Outline each uninfected red blood cell.
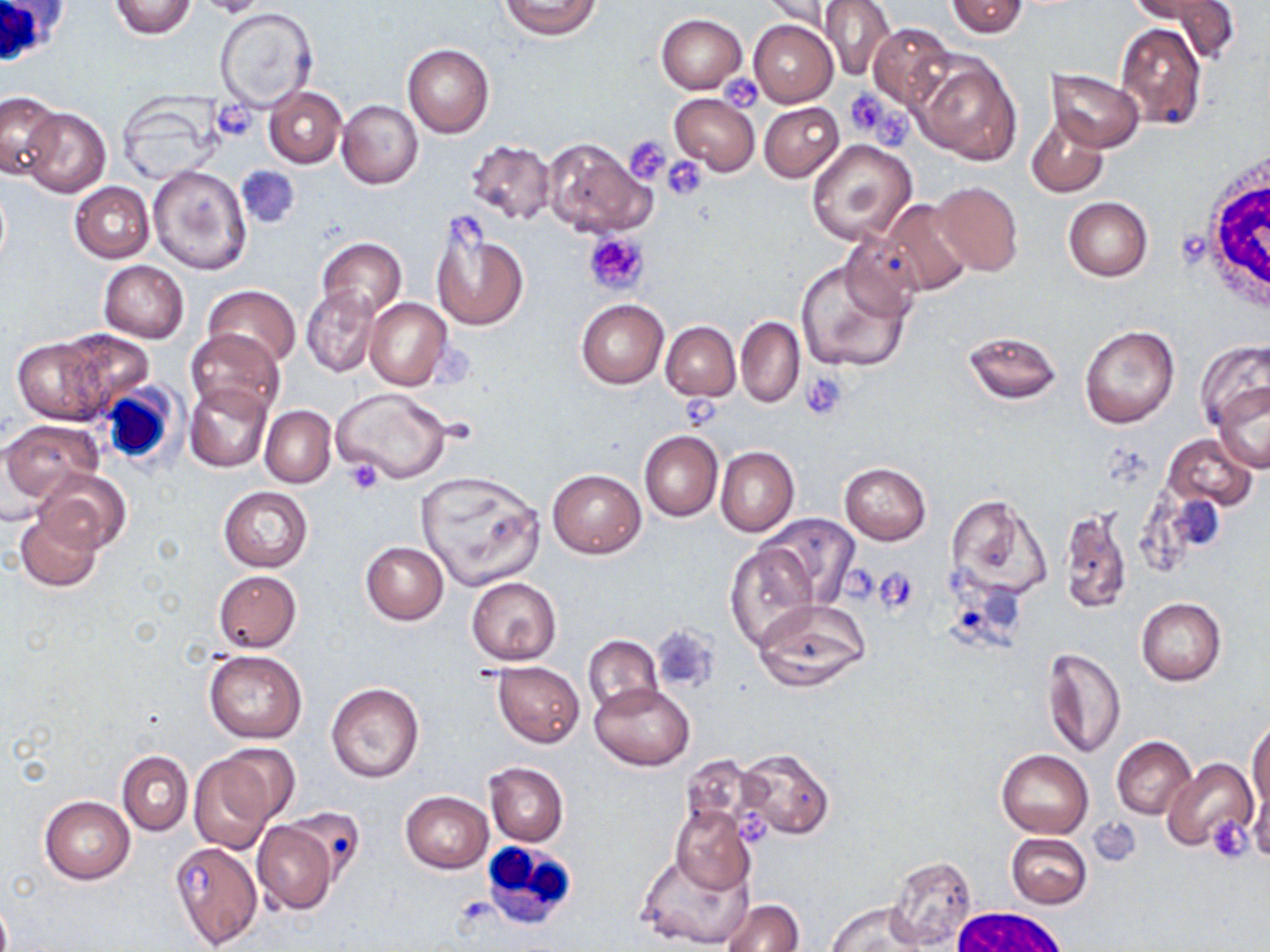

Approximate bounding boxes as named x1/y1/x2/y2 corners in pixels.
Uninfected red blood cells: (x1=108, y1=0, x2=197, y2=40), (x1=500, y1=0, x2=603, y2=42), (x1=760, y1=0, x2=845, y2=32), (x1=820, y1=0, x2=897, y2=83), (x1=945, y1=0, x2=1028, y2=37), (x1=1131, y1=0, x2=1226, y2=27), (x1=1147, y1=0, x2=1240, y2=61), (x1=215, y1=8, x2=317, y2=111), (x1=657, y1=14, x2=747, y2=93), (x1=749, y1=19, x2=838, y2=106), (x1=1116, y1=22, x2=1207, y2=130), (x1=868, y1=23, x2=953, y2=108), (x1=402, y1=44, x2=494, y2=137), (x1=913, y1=53, x2=1022, y2=165), (x1=1048, y1=69, x2=1144, y2=151), (x1=264, y1=87, x2=345, y2=167), (x1=0, y1=91, x2=63, y2=177), (x1=670, y1=93, x2=760, y2=176), (x1=116, y1=94, x2=221, y2=184), (x1=337, y1=100, x2=423, y2=189), (x1=759, y1=101, x2=843, y2=182), (x1=20, y1=108, x2=110, y2=197), (x1=1027, y1=115, x2=1110, y2=199), (x1=540, y1=137, x2=655, y2=239), (x1=464, y1=139, x2=557, y2=225), (x1=806, y1=139, x2=917, y2=246), (x1=235, y1=164, x2=302, y2=229), (x1=148, y1=165, x2=250, y2=274), (x1=933, y1=180, x2=1024, y2=276), (x1=70, y1=182, x2=155, y2=262), (x1=1064, y1=197, x2=1152, y2=282), (x1=880, y1=199, x2=974, y2=296), (x1=432, y1=223, x2=528, y2=332), (x1=838, y1=234, x2=924, y2=318), (x1=316, y1=237, x2=406, y2=322), (x1=796, y1=256, x2=910, y2=373), (x1=99, y1=260, x2=189, y2=342), (x1=301, y1=284, x2=381, y2=378), (x1=202, y1=285, x2=300, y2=369), (x1=364, y1=299, x2=452, y2=390), (x1=576, y1=299, x2=668, y2=389), (x1=736, y1=317, x2=804, y2=407), (x1=661, y1=322, x2=740, y2=400), (x1=1080, y1=325, x2=1181, y2=429), (x1=185, y1=327, x2=284, y2=420), (x1=54, y1=329, x2=154, y2=415), (x1=964, y1=329, x2=1062, y2=405), (x1=12, y1=337, x2=110, y2=424), (x1=1197, y1=339, x2=1270, y2=437), (x1=184, y1=383, x2=271, y2=472), (x1=1212, y1=383, x2=1270, y2=474), (x1=333, y1=387, x2=451, y2=485), (x1=260, y1=405, x2=335, y2=487), (x1=4, y1=419, x2=102, y2=503), (x1=639, y1=431, x2=723, y2=521), (x1=1163, y1=434, x2=1257, y2=511), (x1=716, y1=446, x2=799, y2=536), (x1=838, y1=462, x2=932, y2=544), (x1=36, y1=469, x2=130, y2=553), (x1=548, y1=469, x2=646, y2=558), (x1=415, y1=471, x2=548, y2=591), (x1=219, y1=487, x2=313, y2=572), (x1=944, y1=493, x2=1050, y2=601), (x1=1056, y1=506, x2=1133, y2=615), (x1=15, y1=510, x2=101, y2=592), (x1=760, y1=513, x2=859, y2=609), (x1=361, y1=541, x2=448, y2=624), (x1=726, y1=541, x2=815, y2=650), (x1=213, y1=570, x2=302, y2=653), (x1=478, y1=576, x2=569, y2=747), (x1=466, y1=578, x2=561, y2=665), (x1=1135, y1=596, x2=1226, y2=686), (x1=752, y1=600, x2=870, y2=691), (x1=582, y1=634, x2=662, y2=717), (x1=1043, y1=647, x2=1126, y2=759), (x1=205, y1=650, x2=306, y2=742), (x1=493, y1=662, x2=584, y2=747), (x1=590, y1=682, x2=694, y2=769), (x1=326, y1=683, x2=424, y2=784), (x1=1248, y1=718, x2=1270, y2=812), (x1=1112, y1=736, x2=1196, y2=819), (x1=213, y1=743, x2=301, y2=828), (x1=735, y1=748, x2=834, y2=839), (x1=996, y1=749, x2=1094, y2=838), (x1=116, y1=751, x2=193, y2=835), (x1=186, y1=752, x2=280, y2=855), (x1=1163, y1=757, x2=1258, y2=854), (x1=485, y1=762, x2=569, y2=846), (x1=1245, y1=786, x2=1270, y2=862), (x1=401, y1=791, x2=493, y2=873), (x1=39, y1=796, x2=135, y2=884), (x1=670, y1=805, x2=754, y2=894), (x1=283, y1=808, x2=365, y2=888), (x1=250, y1=819, x2=338, y2=914), (x1=1007, y1=832, x2=1092, y2=909), (x1=168, y1=841, x2=263, y2=948), (x1=636, y1=846, x2=752, y2=947), (x1=887, y1=855, x2=977, y2=950), (x1=722, y1=899, x2=804, y2=952), (x1=825, y1=901, x2=933, y2=952).

slide-level diagnosis = negative for blood parasites
preparation = thin blood smear
modality = light microscopy
magnification = 1000x
field of view = one of a larger specimen
stain = May-Grünwald-Giemsa
white blood cell locations = approximate bounding boxes as named x1/y1/x2/y2 corners in pixels: (x1=0, y1=1, x2=67, y2=73), (x1=1192, y1=142, x2=1270, y2=317), (x1=97, y1=383, x2=181, y2=468), (x1=481, y1=838, x2=580, y2=929), (x1=953, y1=905, x2=1069, y2=952)
platelet locations = approximate bounding boxes as named x1/y1/x2/y2 corners in pixels: (x1=720, y1=73, x2=764, y2=112), (x1=846, y1=90, x2=912, y2=147), (x1=213, y1=100, x2=256, y2=141), (x1=625, y1=135, x2=671, y2=186), (x1=661, y1=156, x2=709, y2=200), (x1=582, y1=231, x2=650, y2=295), (x1=800, y1=371, x2=849, y2=420), (x1=682, y1=391, x2=725, y2=435), (x1=343, y1=457, x2=386, y2=496), (x1=842, y1=563, x2=878, y2=606), (x1=874, y1=567, x2=918, y2=613), (x1=650, y1=626, x2=720, y2=694), (x1=737, y1=808, x2=771, y2=846), (x1=1207, y1=815, x2=1254, y2=863), (x1=1089, y1=819, x2=1141, y2=866)
image size = 1270×952 pixels